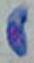 Photomicrograph. Toxoplasma gondii is shown. Captured at 1000x magnification.